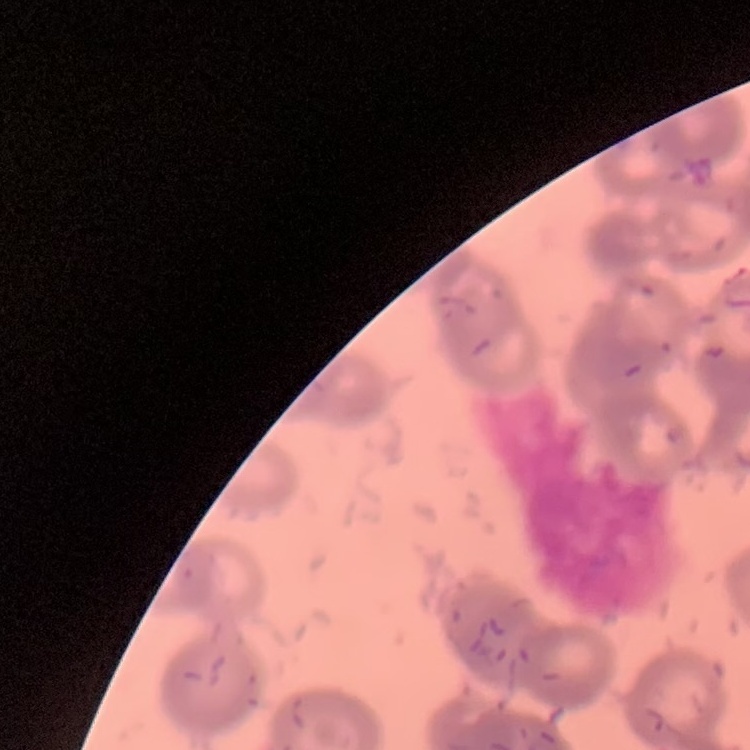
erythrocyte morphology = rouleaux formation
image type = square crop of a larger photomicrograph
preparation = thin peripheral smear
stain = Field's or Giemsa